Report the malaria status of this cell.
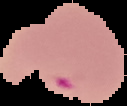
It is parasitized.

Summary:
  - Image type: cell region segmented out of the field of view; surrounding area masked to black
  - Image size: 127×106 pixels
  - Preparation: thin blood film